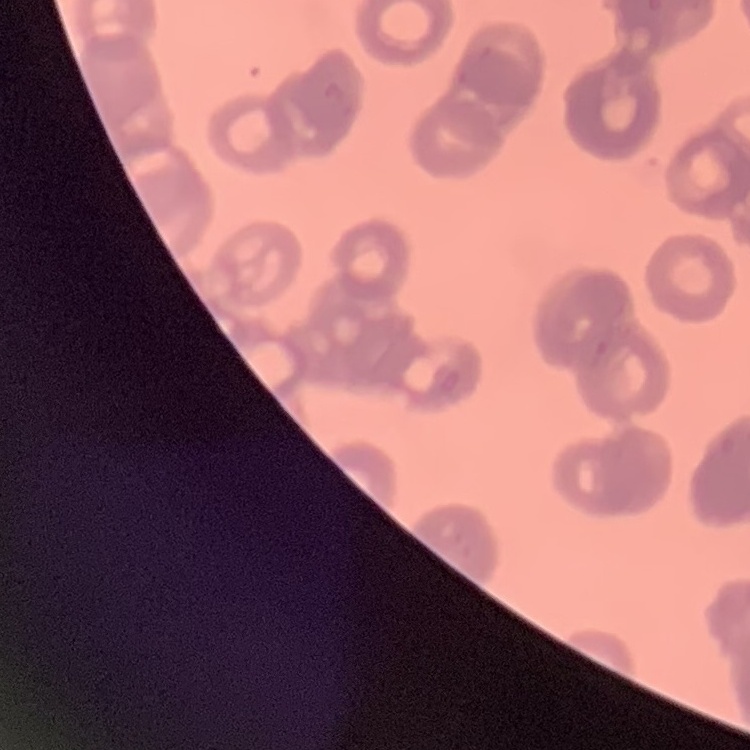
{
  "red_blood_cell_morphology": "rouleaux formation",
  "stain": "Field's or Giemsa",
  "preparation": "thin peripheral smear",
  "image_type": "one tile cut from a larger photomicrograph"
}